Comment on the morphology of the red blood cells.
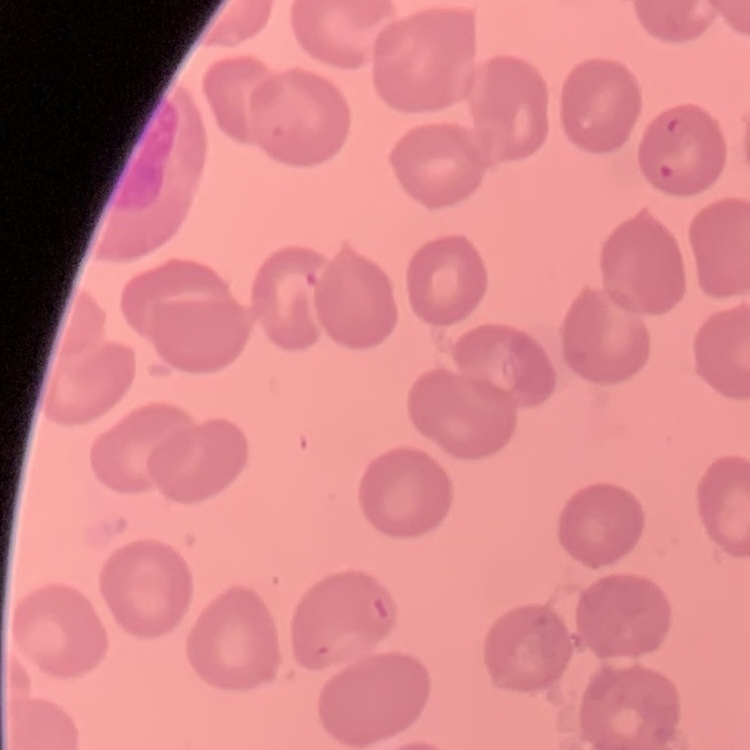
No rouleaux formation.

Thin peripheral smear. One tile cut from a larger photomicrograph. Field's or Giemsa stain.